Assess this cell for malaria.
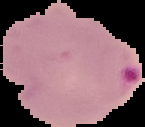
Parasitized.

image size = 145×127 pixels
image type = segmented cell region on a black background
preparation = thin blood smear